Comment on the morphology of the erythrocytes.
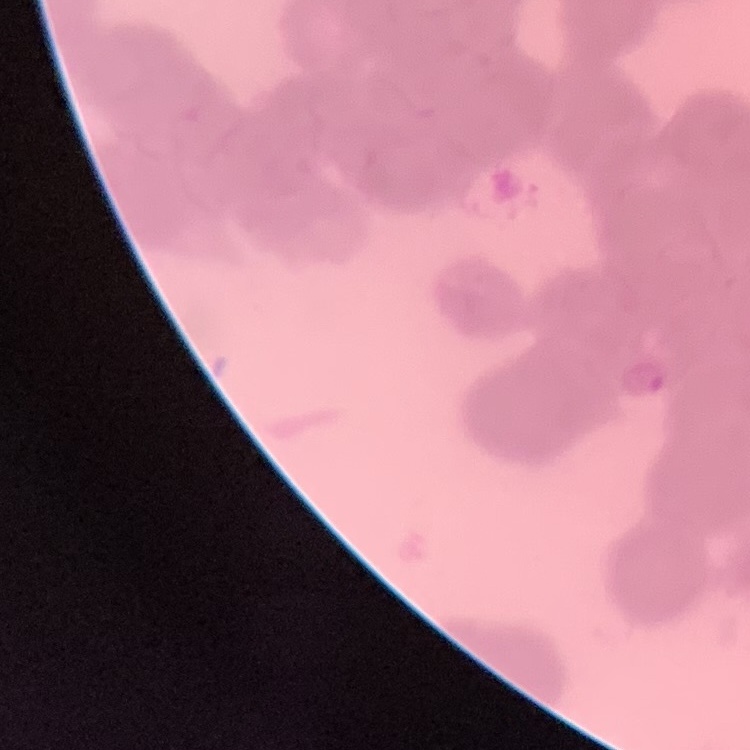

They show rouleaux formation.

stain = Field's or Giemsa
image type = one tile cut from a larger photomicrograph
preparation = thin blood film